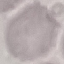
malaria status = uninfected
capture = smartphone through the microscope eyepiece
preparation = thin smear
stain = Giemsa
image type = cell patch, automatically extracted from a larger field of view and resized to 64 × 64 pixels